Outline each uninfected red blood cell.
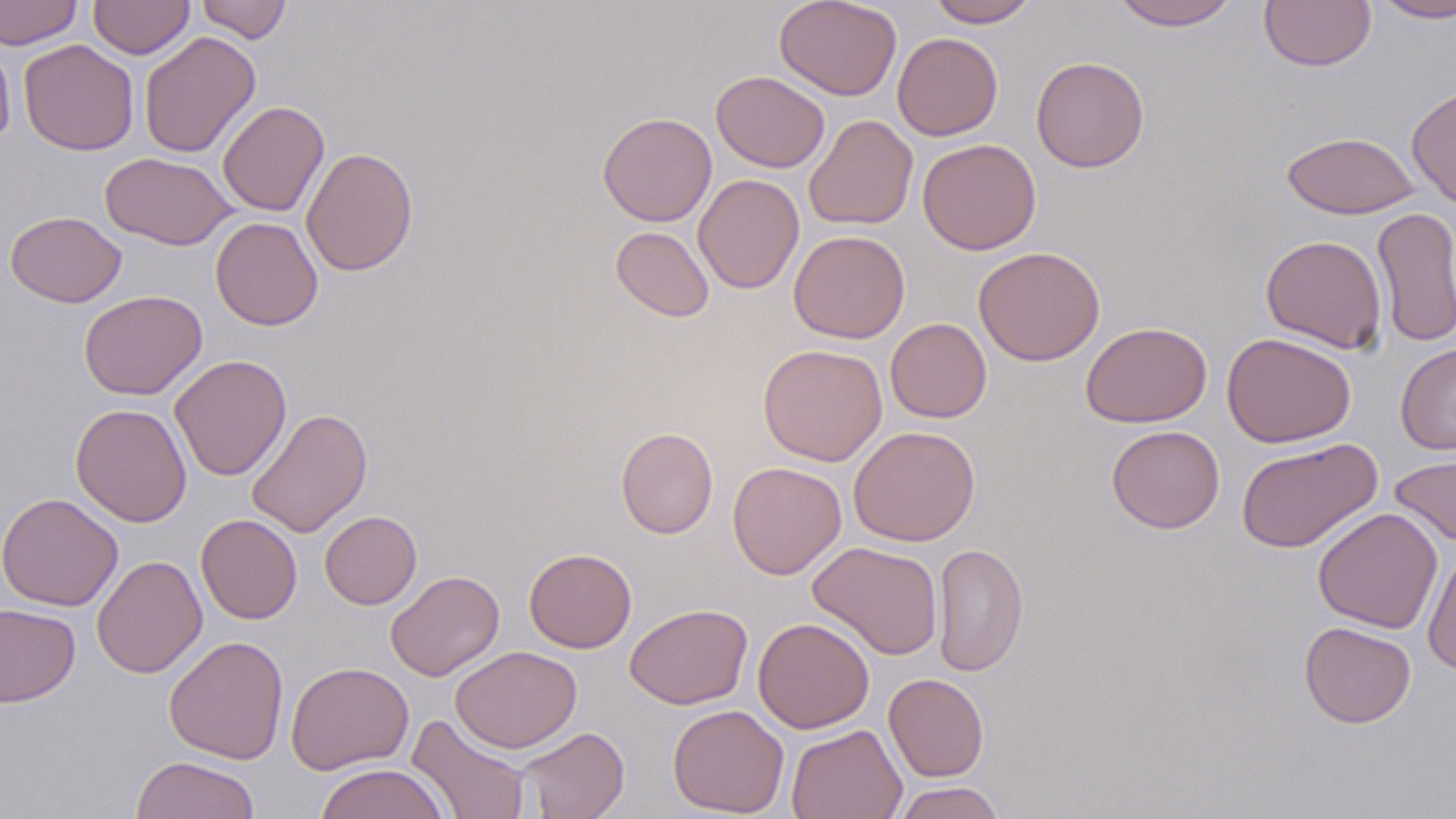

Approximate bounding boxes as named x1/y1/x2/y2 corners in pixels.
Uninfected red blood cells: (x1=0, y1=0, x2=83, y2=49), (x1=88, y1=0, x2=194, y2=59), (x1=195, y1=0, x2=292, y2=43), (x1=774, y1=0, x2=902, y2=101), (x1=927, y1=0, x2=1038, y2=28), (x1=1109, y1=0, x2=1240, y2=30), (x1=1259, y1=0, x2=1376, y2=72), (x1=1371, y1=0, x2=1456, y2=22), (x1=138, y1=31, x2=261, y2=158), (x1=892, y1=32, x2=1003, y2=141), (x1=0, y1=34, x2=16, y2=148), (x1=18, y1=39, x2=139, y2=155), (x1=1031, y1=55, x2=1150, y2=173), (x1=711, y1=70, x2=830, y2=173), (x1=1406, y1=84, x2=1456, y2=210), (x1=217, y1=100, x2=329, y2=217), (x1=597, y1=111, x2=717, y2=227), (x1=804, y1=114, x2=918, y2=231), (x1=1281, y1=131, x2=1420, y2=219), (x1=917, y1=138, x2=1041, y2=255), (x1=300, y1=147, x2=418, y2=276), (x1=99, y1=152, x2=236, y2=250), (x1=693, y1=173, x2=804, y2=294), (x1=1371, y1=207, x2=1456, y2=348), (x1=5, y1=211, x2=126, y2=307), (x1=210, y1=216, x2=323, y2=331), (x1=610, y1=226, x2=714, y2=322), (x1=788, y1=230, x2=910, y2=344), (x1=1261, y1=235, x2=1387, y2=353), (x1=973, y1=246, x2=1105, y2=366), (x1=78, y1=289, x2=207, y2=400), (x1=885, y1=317, x2=992, y2=423), (x1=1081, y1=321, x2=1212, y2=427), (x1=1222, y1=332, x2=1356, y2=448), (x1=758, y1=343, x2=888, y2=467), (x1=1395, y1=343, x2=1456, y2=454), (x1=169, y1=355, x2=292, y2=481), (x1=70, y1=403, x2=192, y2=527), (x1=245, y1=407, x2=373, y2=538), (x1=848, y1=425, x2=980, y2=546), (x1=1106, y1=425, x2=1225, y2=533), (x1=615, y1=426, x2=718, y2=538), (x1=1235, y1=437, x2=1382, y2=553), (x1=1389, y1=450, x2=1456, y2=548), (x1=727, y1=461, x2=846, y2=579), (x1=1, y1=492, x2=123, y2=611), (x1=1313, y1=507, x2=1442, y2=634), (x1=319, y1=510, x2=422, y2=609), (x1=196, y1=514, x2=302, y2=624), (x1=807, y1=541, x2=944, y2=660), (x1=932, y1=542, x2=1029, y2=677), (x1=1423, y1=547, x2=1456, y2=678), (x1=523, y1=548, x2=637, y2=653), (x1=91, y1=555, x2=207, y2=679), (x1=385, y1=570, x2=504, y2=681), (x1=0, y1=603, x2=80, y2=708), (x1=624, y1=603, x2=753, y2=709), (x1=752, y1=617, x2=874, y2=733), (x1=1299, y1=621, x2=1416, y2=728), (x1=163, y1=635, x2=289, y2=765), (x1=450, y1=645, x2=581, y2=752), (x1=286, y1=660, x2=414, y2=775), (x1=884, y1=673, x2=989, y2=782), (x1=667, y1=704, x2=789, y2=817), (x1=406, y1=713, x2=532, y2=819), (x1=786, y1=724, x2=907, y2=819), (x1=513, y1=726, x2=630, y2=818), (x1=131, y1=755, x2=262, y2=819), (x1=315, y1=763, x2=451, y2=819), (x1=893, y1=782, x2=1006, y2=819).

Summary:
  - Slide-level diagnosis: no evidence of blood parasites
  - Image size: 1456×819 pixels
  - Field of view: one of a larger specimen
  - Preparation: thin blood smear
  - Magnification: 1000x
  - Modality: light microscopy
  - Stain: May-Grünwald-Giemsa